Give the position of every malaria parasite.
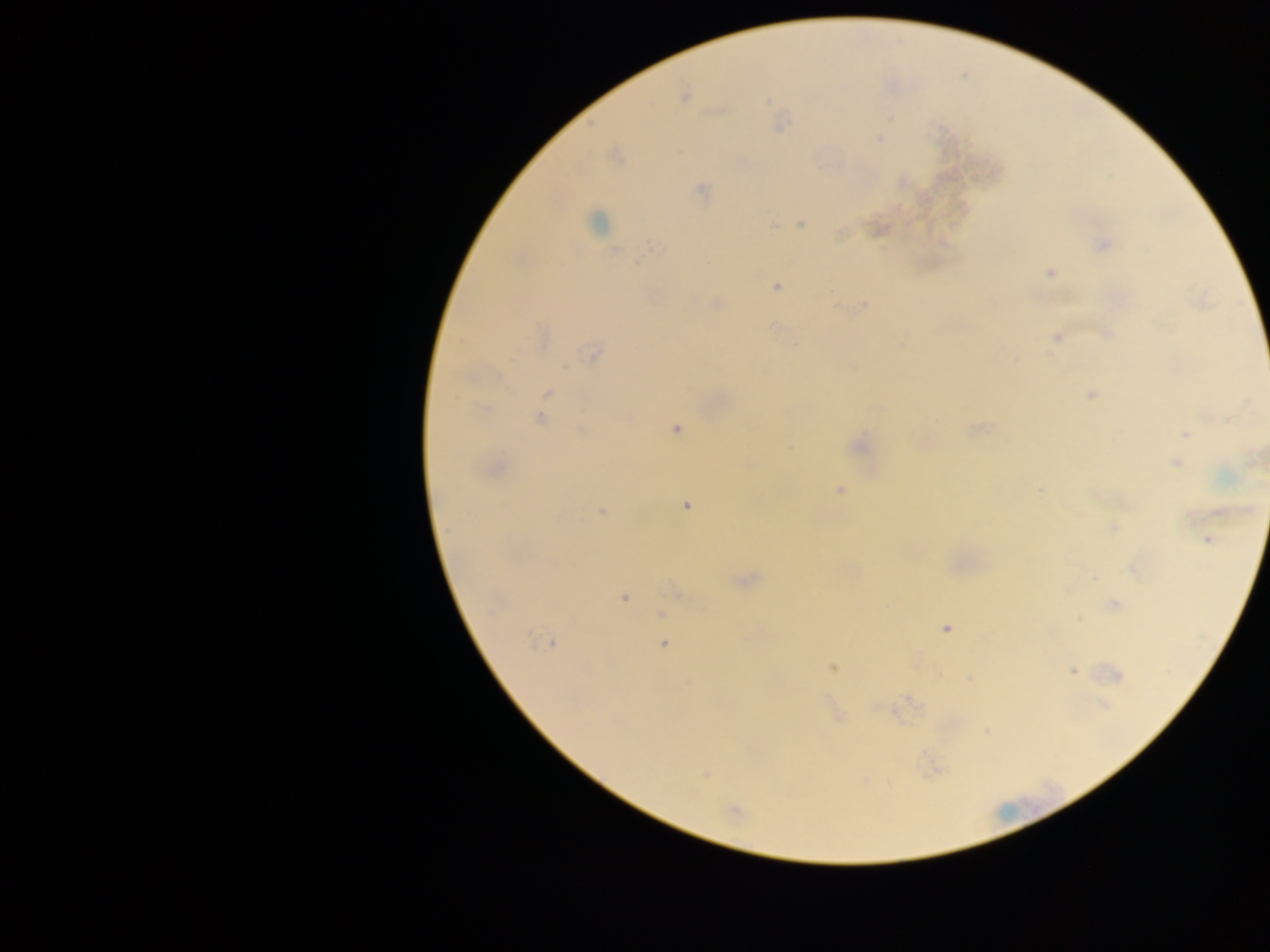

Approximate centers as {x, y} in pixels.
Malaria parasites: {685, 96}, {766, 102}, {890, 119}, {879, 139}, {701, 190}, {801, 223}, {772, 224}, {873, 227}, {840, 234}, {1102, 244}, {652, 247}, {637, 262}, {1051, 273}, {719, 302}, {865, 304}, {836, 308}, {775, 327}, {1056, 338}, {794, 344}, {594, 353}, {565, 367}, {545, 393}, {1089, 394}, {539, 418}, {977, 426}, {677, 430}, {1184, 434}, {919, 440}, {926, 441}, {862, 442}, {1177, 464}, {840, 488}, {1041, 489}, {686, 504}, {602, 512}, {1134, 570}, {1093, 577}, {749, 579}, {672, 590}, {624, 598}, {1116, 604}, {1078, 619}, {661, 620}, {945, 629}, {552, 641}, {663, 644}, {832, 668}, {1073, 672}, {1118, 675}, {908, 697}, {886, 709}, {707, 774}, {736, 808}.

Image is 1270×952 pixels. Collected in Ghana. Thick blood film. Single field of view. Mobile-phone photograph taken through the microscope.